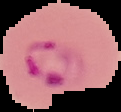
image type = segmented cell region on a black background
malaria status = parasitized
image size = 121×112 pixels
preparation = thin blood film